Identify the cell.
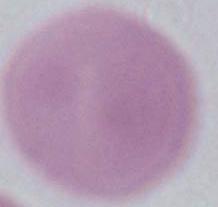
This is an erythrocyte.

Captured at 1000x magnification. Micrograph.